Classify this cell by malaria status.
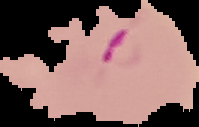

Parasitized.

Summary:
  - Preparation: thin blood smear
  - Image size: 199×127 pixels
  - Image type: segmented cell region with the area outside set to black